Assess the morphology of the erythrocytes.
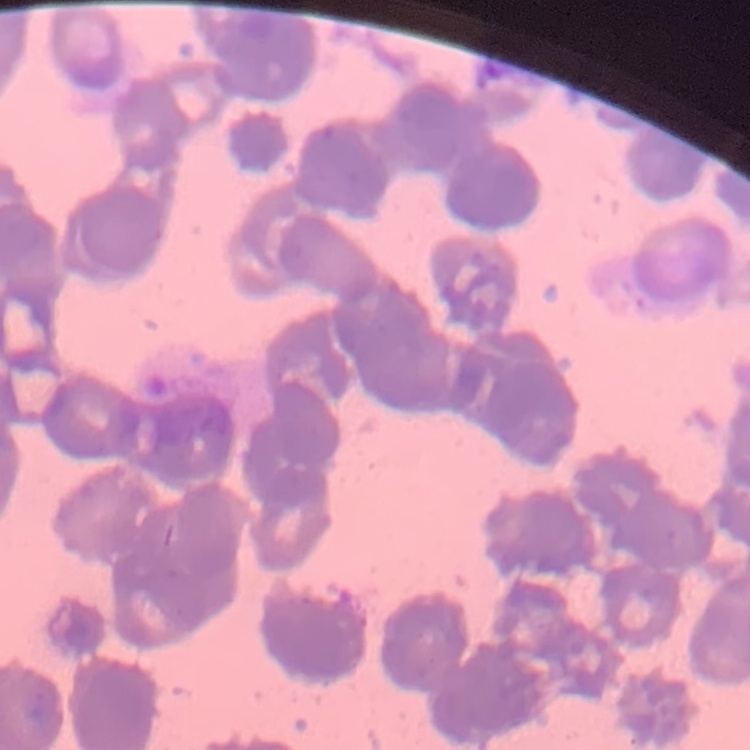
They show rouleaux formation.

image_type: square crop of a larger photomicrograph
preparation: thin peripheral smear
stain: Field's or Giemsa